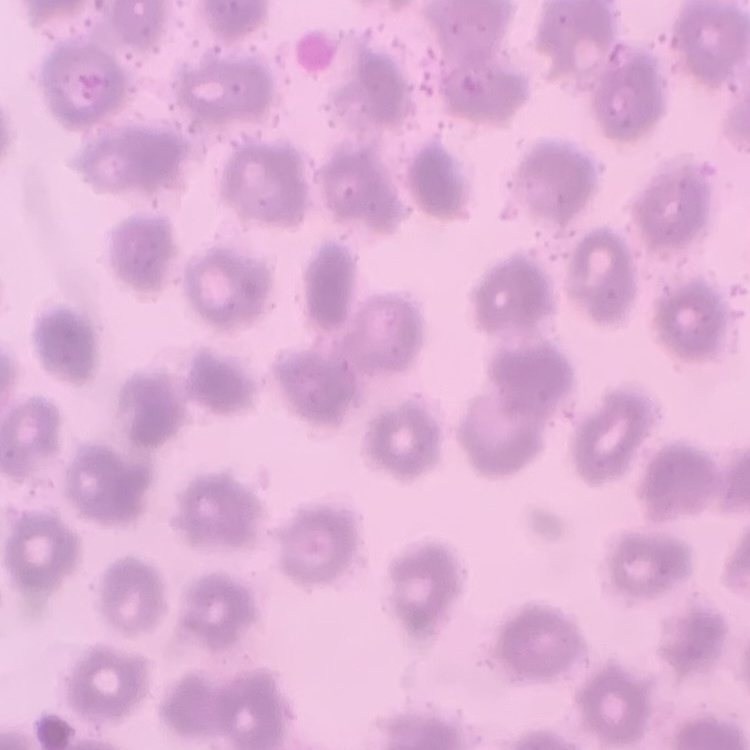

Summary:
  - Erythrocyte morphology: no rouleaux formation
  - Stain: Field's or Giemsa
  - Preparation: thin blood smear
  - Image type: square crop of a larger photomicrograph